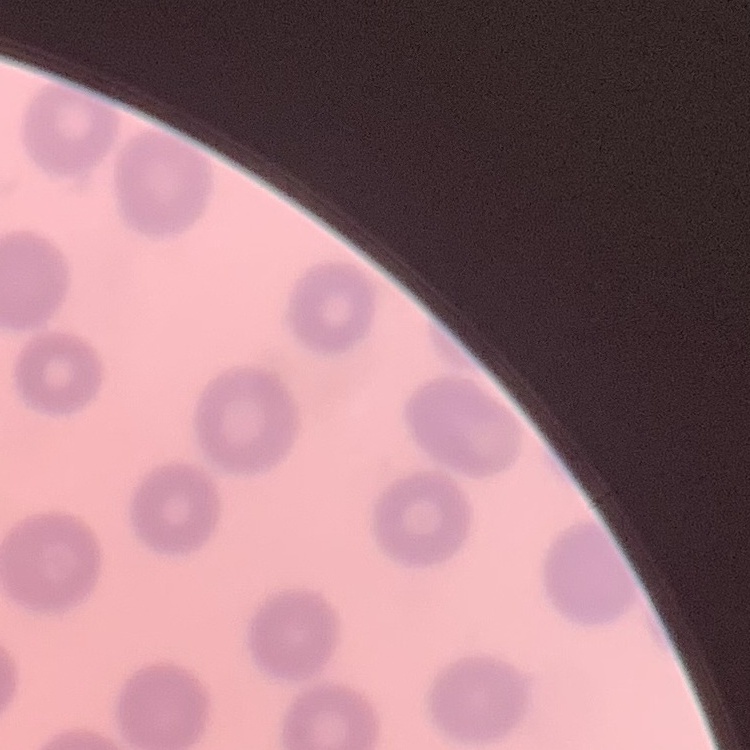
The red blood cells show no rouleaux formation. One tile cut from a larger photomicrograph. Stained with either Field's or Giemsa. Thin blood smear.